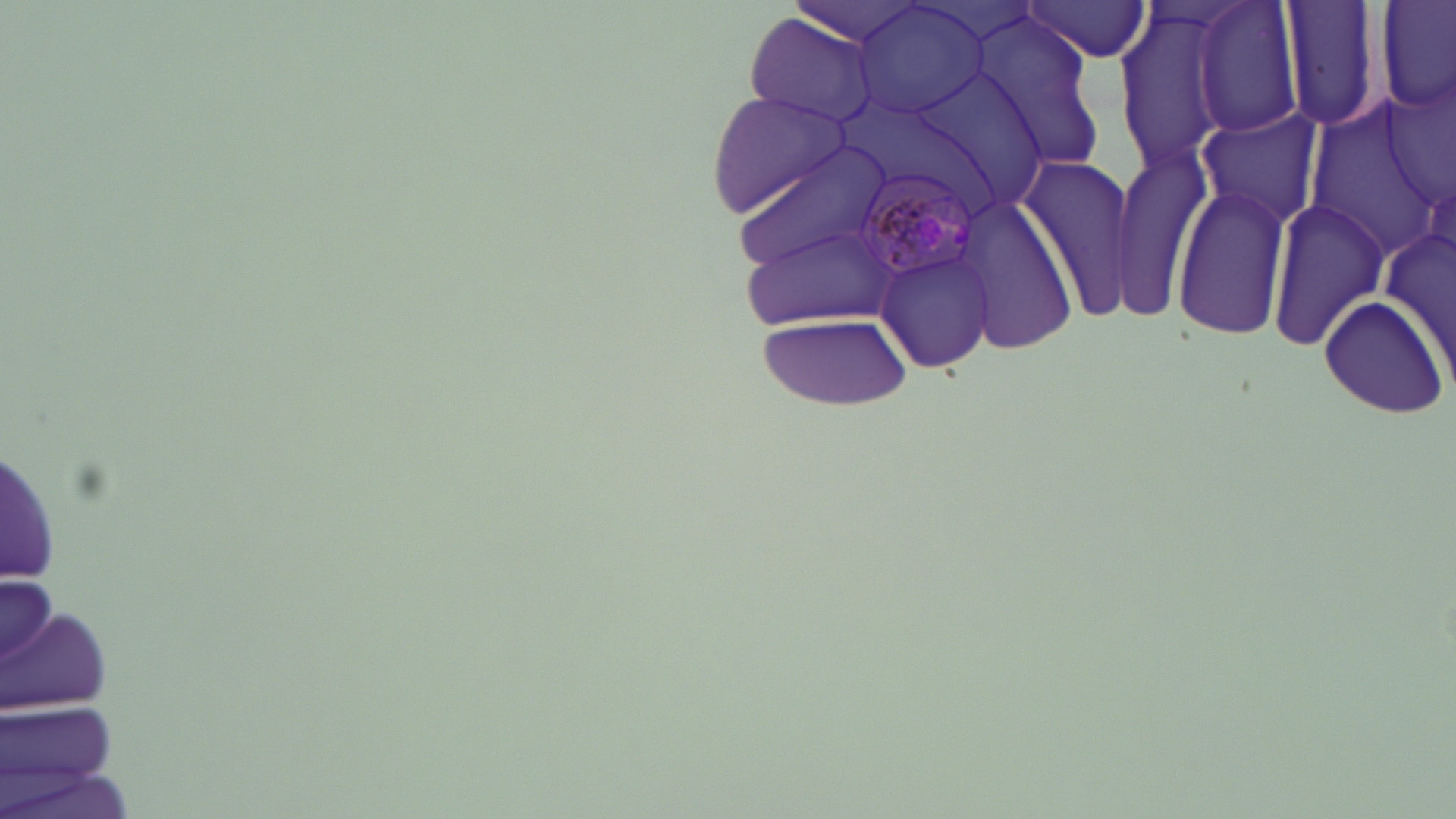

Approximate bounding boxes as [x1, y1, x2, y2] in pixels. Uninfected red blood cell locations: [1014, 0, 1156, 67], [1281, 0, 1383, 133], [1374, 0, 1454, 120], [1189, 1, 1307, 142], [851, 2, 992, 119], [1110, 8, 1238, 171], [741, 11, 884, 130], [965, 14, 1107, 176], [908, 62, 1057, 212], [704, 90, 849, 218], [1302, 103, 1447, 258], [1193, 107, 1322, 228], [726, 141, 893, 275], [1107, 154, 1209, 324], [1014, 155, 1139, 325], [1170, 184, 1292, 338], [952, 197, 1079, 355], [1266, 198, 1395, 347], [1380, 214, 1456, 378], [741, 223, 904, 337], [875, 243, 1001, 374], [1317, 294, 1450, 422], [754, 308, 915, 414], [0, 446, 60, 591], [7, 589, 113, 721], [4, 695, 126, 807]. Plasmodium malariae-infected red blood cell locations: [851, 155, 988, 286]. Slide-level diagnosis: Plasmodium malariae. One field of a larger specimen. Light microscopy. Thin blood film. Image is 1456×819 pixels. Captured at 1000x magnification. May-Grünwald-Giemsa-stained preparation.